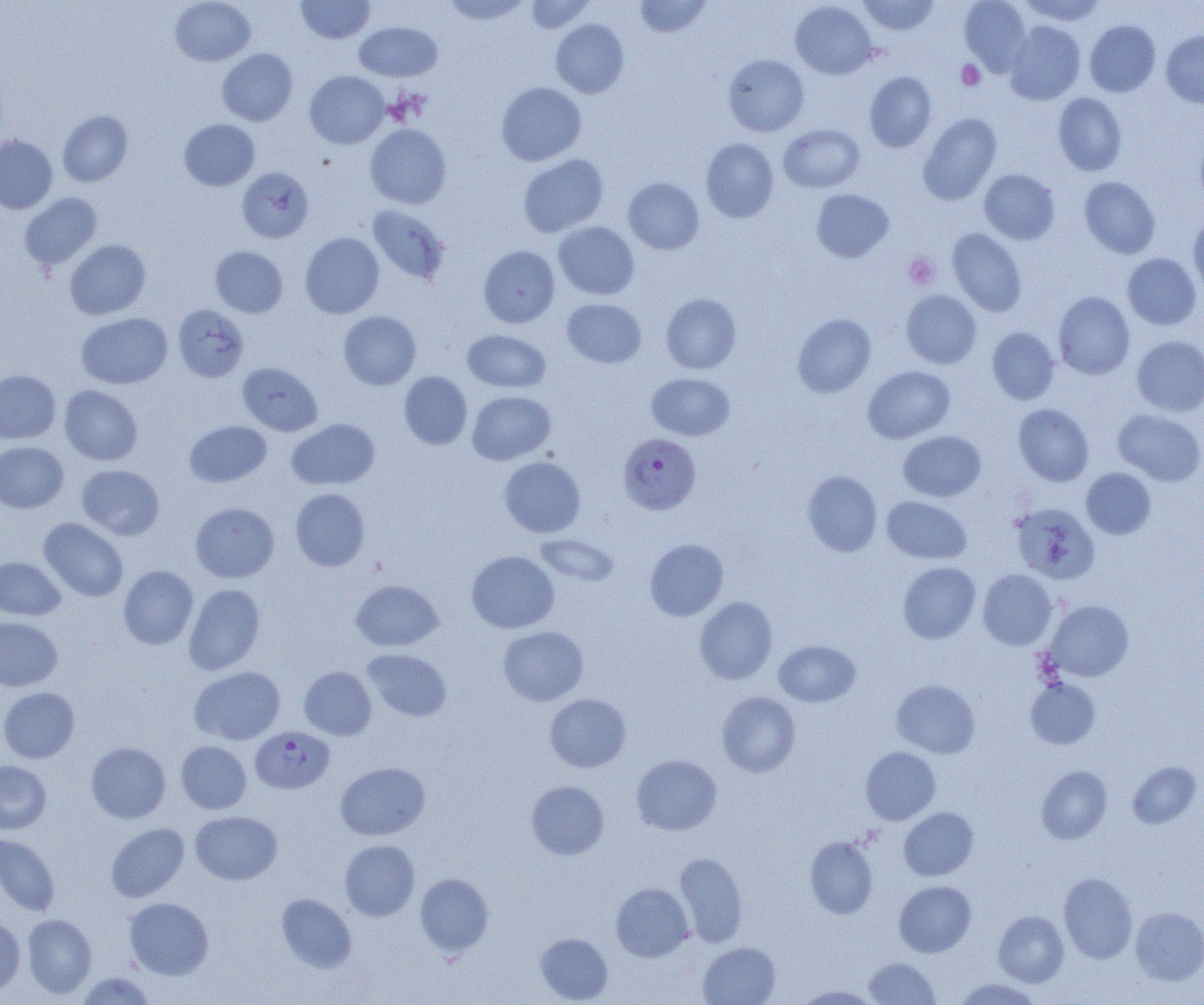 Approximate bounding boxes as named x1/y1/x2/y2 corners in pixels. Uninfected red blood cell locations: (x1=170, y1=0, x2=256, y2=66), (x1=296, y1=0, x2=374, y2=44), (x1=441, y1=0, x2=532, y2=25), (x1=524, y1=0, x2=595, y2=33), (x1=634, y1=0, x2=713, y2=37), (x1=858, y1=0, x2=940, y2=35), (x1=959, y1=0, x2=1032, y2=75), (x1=1019, y1=0, x2=1107, y2=25), (x1=789, y1=1, x2=877, y2=79), (x1=551, y1=18, x2=629, y2=98), (x1=1084, y1=20, x2=1161, y2=97), (x1=354, y1=21, x2=442, y2=81), (x1=1004, y1=21, x2=1086, y2=105), (x1=1161, y1=31, x2=1204, y2=107), (x1=217, y1=48, x2=297, y2=126), (x1=723, y1=54, x2=809, y2=136), (x1=305, y1=71, x2=389, y2=149), (x1=864, y1=71, x2=937, y2=152), (x1=496, y1=81, x2=587, y2=166), (x1=1053, y1=93, x2=1127, y2=176), (x1=57, y1=110, x2=133, y2=187), (x1=918, y1=113, x2=1002, y2=205), (x1=178, y1=119, x2=260, y2=191), (x1=365, y1=123, x2=452, y2=209), (x1=778, y1=124, x2=865, y2=193), (x1=0, y1=135, x2=57, y2=214), (x1=701, y1=138, x2=779, y2=223), (x1=518, y1=154, x2=609, y2=238), (x1=237, y1=167, x2=313, y2=243), (x1=979, y1=168, x2=1060, y2=245), (x1=1079, y1=176, x2=1161, y2=258), (x1=623, y1=177, x2=704, y2=254), (x1=811, y1=188, x2=894, y2=263), (x1=20, y1=193, x2=102, y2=271), (x1=367, y1=206, x2=449, y2=284), (x1=1188, y1=213, x2=1204, y2=297), (x1=553, y1=221, x2=640, y2=300), (x1=947, y1=228, x2=1028, y2=317), (x1=300, y1=232, x2=384, y2=318), (x1=65, y1=239, x2=151, y2=320), (x1=478, y1=245, x2=560, y2=328), (x1=210, y1=246, x2=288, y2=318), (x1=1122, y1=253, x2=1202, y2=330), (x1=901, y1=289, x2=982, y2=369), (x1=1053, y1=291, x2=1135, y2=380), (x1=661, y1=293, x2=742, y2=374), (x1=561, y1=298, x2=646, y2=368), (x1=173, y1=304, x2=249, y2=382), (x1=338, y1=311, x2=421, y2=390), (x1=77, y1=313, x2=172, y2=389), (x1=792, y1=313, x2=876, y2=398), (x1=987, y1=327, x2=1059, y2=404), (x1=463, y1=330, x2=551, y2=393), (x1=1132, y1=336, x2=1204, y2=416), (x1=237, y1=362, x2=322, y2=436), (x1=863, y1=366, x2=956, y2=443), (x1=0, y1=370, x2=60, y2=444), (x1=399, y1=371, x2=472, y2=450), (x1=647, y1=373, x2=735, y2=440), (x1=59, y1=385, x2=143, y2=465), (x1=467, y1=391, x2=556, y2=465), (x1=1013, y1=404, x2=1094, y2=486), (x1=1113, y1=409, x2=1204, y2=486), (x1=287, y1=418, x2=380, y2=490), (x1=185, y1=421, x2=271, y2=487), (x1=898, y1=430, x2=986, y2=501), (x1=0, y1=441, x2=68, y2=513), (x1=499, y1=456, x2=586, y2=537), (x1=77, y1=465, x2=164, y2=540), (x1=1081, y1=468, x2=1156, y2=539), (x1=803, y1=470, x2=882, y2=557), (x1=290, y1=488, x2=370, y2=571), (x1=882, y1=496, x2=972, y2=564), (x1=190, y1=502, x2=279, y2=582), (x1=1011, y1=502, x2=1100, y2=584), (x1=39, y1=518, x2=128, y2=602), (x1=534, y1=533, x2=619, y2=587), (x1=645, y1=538, x2=729, y2=620), (x1=466, y1=550, x2=559, y2=633), (x1=0, y1=556, x2=65, y2=620), (x1=898, y1=561, x2=981, y2=644), (x1=118, y1=566, x2=198, y2=649), (x1=978, y1=569, x2=1057, y2=649), (x1=351, y1=579, x2=443, y2=651), (x1=183, y1=584, x2=265, y2=675), (x1=694, y1=596, x2=778, y2=684), (x1=1044, y1=600, x2=1134, y2=682), (x1=0, y1=617, x2=63, y2=691), (x1=498, y1=626, x2=589, y2=705), (x1=773, y1=640, x2=861, y2=707), (x1=363, y1=649, x2=452, y2=722), (x1=190, y1=666, x2=285, y2=745), (x1=299, y1=666, x2=376, y2=740), (x1=1026, y1=678, x2=1101, y2=749), (x1=891, y1=679, x2=981, y2=758), (x1=0, y1=687, x2=79, y2=763), (x1=716, y1=692, x2=801, y2=777), (x1=544, y1=693, x2=631, y2=772), (x1=176, y1=740, x2=251, y2=814), (x1=85, y1=742, x2=171, y2=823), (x1=861, y1=747, x2=940, y2=825), (x1=631, y1=754, x2=722, y2=835), (x1=0, y1=760, x2=51, y2=834), (x1=1127, y1=761, x2=1202, y2=829), (x1=335, y1=762, x2=430, y2=841), (x1=1036, y1=766, x2=1113, y2=844), (x1=526, y1=781, x2=609, y2=859), (x1=898, y1=807, x2=979, y2=881), (x1=190, y1=811, x2=282, y2=885), (x1=106, y1=823, x2=189, y2=902), (x1=0, y1=833, x2=60, y2=916), (x1=805, y1=836, x2=878, y2=919), (x1=339, y1=840, x2=420, y2=920), (x1=675, y1=852, x2=748, y2=947), (x1=1058, y1=872, x2=1138, y2=963), (x1=414, y1=873, x2=494, y2=957), (x1=894, y1=881, x2=976, y2=957), (x1=611, y1=882, x2=694, y2=962), (x1=276, y1=894, x2=356, y2=972), (x1=124, y1=897, x2=214, y2=980), (x1=1131, y1=906, x2=1204, y2=985), (x1=993, y1=910, x2=1069, y2=986), (x1=22, y1=914, x2=97, y2=998), (x1=0, y1=918, x2=25, y2=996), (x1=535, y1=933, x2=613, y2=1004), (x1=698, y1=942, x2=780, y2=1005), (x1=865, y1=957, x2=940, y2=1004), (x1=75, y1=971, x2=156, y2=1004), (x1=954, y1=977, x2=1042, y2=1005), (x1=796, y1=985, x2=879, y2=1004). Plasmodium falciparum-infected red blood cell locations: (x1=618, y1=433, x2=702, y2=514), (x1=251, y1=726, x2=334, y2=793). Platelet locations: (x1=956, y1=60, x2=986, y2=91), (x1=904, y1=253, x2=940, y2=290). Slide-level diagnosis: Plasmodium falciparum. Thin blood film. Optical microscopy. Single field of view. 1000x magnification. Image is 1204×1005 pixels.